Give the extent of all uninfected red blood cells.
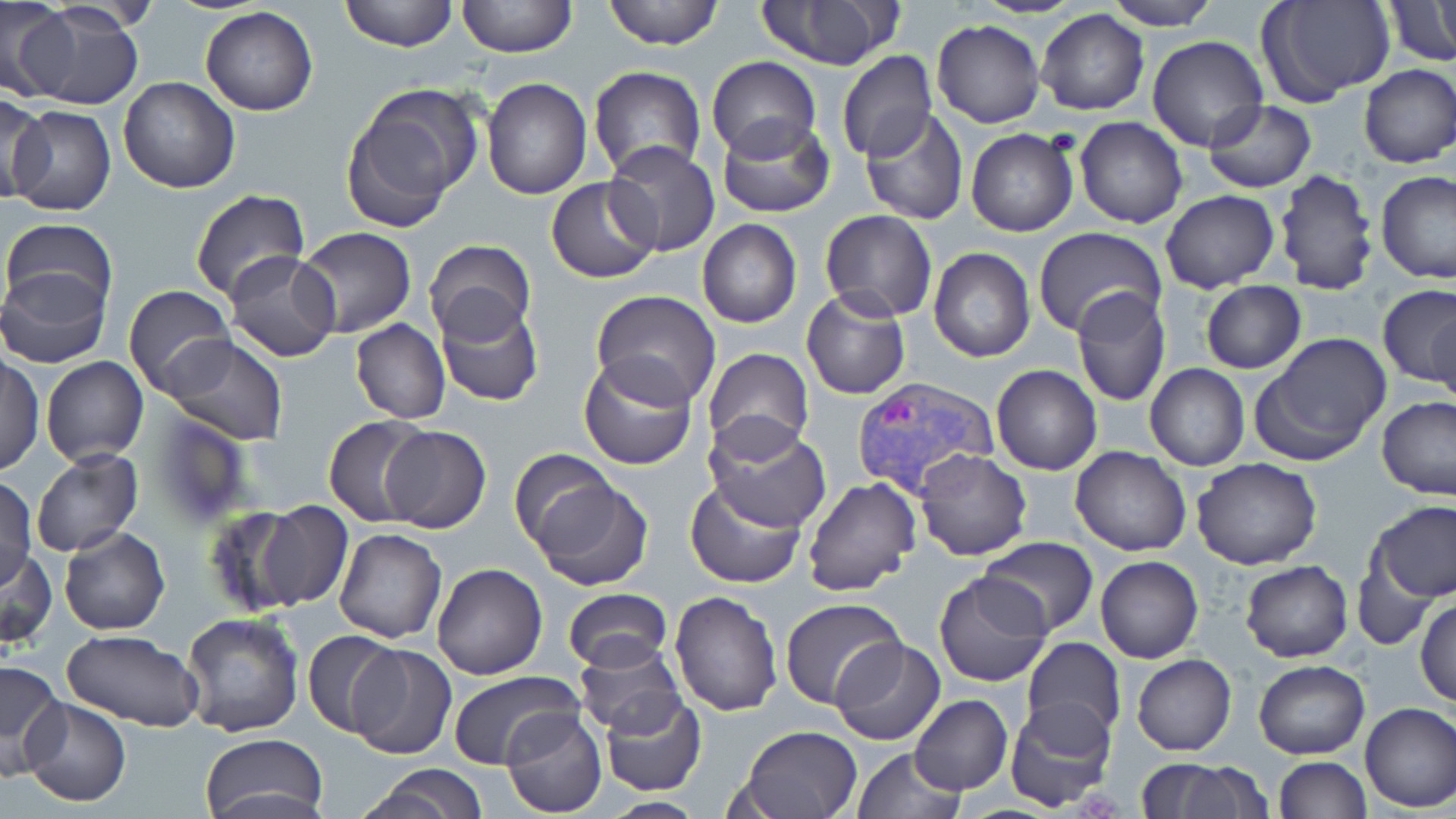
Approximate bounding boxes as (x1, y1, x2, y2) in pixels.
Uninfected red blood cells: (340, 0, 457, 51), (456, 0, 578, 60), (601, 0, 726, 50), (972, 0, 1083, 19), (1106, 0, 1220, 29), (1260, 0, 1395, 109), (1382, 0, 1456, 68), (0, 1, 74, 102), (18, 1, 144, 111), (751, 1, 898, 71), (201, 7, 317, 115), (1036, 8, 1149, 116), (932, 21, 1044, 129), (1148, 36, 1269, 152), (836, 52, 937, 162), (706, 56, 821, 162), (1356, 64, 1455, 168), (588, 65, 706, 179), (118, 76, 239, 193), (482, 77, 593, 200), (340, 85, 481, 227), (0, 93, 53, 202), (1202, 100, 1318, 195), (8, 104, 116, 216), (858, 110, 969, 225), (715, 114, 836, 218), (1074, 117, 1187, 229), (966, 130, 1077, 237), (603, 141, 722, 257), (1273, 167, 1380, 296), (1377, 170, 1456, 285), (545, 177, 659, 284), (187, 189, 312, 307), (1161, 190, 1281, 293), (820, 210, 937, 321), (2, 216, 117, 314), (697, 219, 802, 328), (295, 227, 416, 338), (1032, 227, 1167, 341), (424, 239, 536, 346), (929, 247, 1035, 362), (223, 250, 342, 363), (0, 268, 112, 368), (1199, 281, 1308, 374), (1379, 284, 1456, 388), (122, 285, 238, 398), (800, 288, 912, 400), (1072, 288, 1172, 406), (591, 291, 721, 408), (435, 299, 545, 408), (1429, 302, 1456, 412), (350, 319, 451, 424), (1251, 333, 1392, 466), (162, 335, 289, 445), (704, 347, 814, 456), (577, 353, 698, 469), (1, 354, 44, 478), (41, 356, 148, 465), (991, 364, 1103, 475), (1145, 364, 1249, 471), (1378, 398, 1456, 501), (144, 412, 254, 530), (324, 415, 433, 527), (706, 420, 831, 534), (378, 425, 492, 533), (1070, 446, 1191, 557), (509, 448, 618, 552), (29, 449, 144, 558), (914, 449, 1033, 561), (1192, 457, 1322, 570), (525, 472, 654, 591), (1, 476, 37, 587), (802, 476, 923, 599), (685, 478, 807, 588), (252, 500, 353, 611), (1369, 502, 1455, 602), (200, 504, 315, 616), (59, 527, 169, 635), (334, 527, 447, 643), (978, 536, 1100, 636), (0, 546, 57, 650), (1346, 552, 1439, 651), (1095, 555, 1204, 664), (1240, 560, 1352, 663), (431, 563, 547, 679), (932, 571, 1053, 686), (562, 589, 673, 673), (669, 589, 783, 716), (1415, 597, 1456, 706), (780, 598, 905, 711), (179, 612, 306, 738), (301, 629, 403, 739), (62, 630, 205, 730), (32, 635, 180, 791), (572, 635, 686, 737), (829, 637, 944, 747), (1021, 637, 1126, 746), (348, 643, 457, 760), (1131, 653, 1237, 755), (1254, 660, 1369, 760), (0, 661, 68, 777), (447, 669, 586, 770), (599, 692, 707, 796), (909, 693, 1012, 795), (21, 697, 130, 806), (1004, 698, 1116, 811), (1358, 701, 1456, 813), (500, 707, 608, 816), (733, 725, 862, 819), (198, 734, 330, 819), (851, 746, 965, 819), (1274, 756, 1371, 818), (1144, 761, 1270, 819), (358, 765, 489, 819), (593, 796, 709, 818).

{
  "slide_level_diagnosis": "Plasmodium vivax",
  "preparation": "thin blood smear",
  "magnification": "1000x",
  "field_of_view": "one of a larger specimen",
  "modality": "light microscopy",
  "plasmodium_vivax_infected_red_blood_cell_locations": "approximate bounding boxes as (x1, y1, x2, y2) in pixels: (850, 376, 1000, 499)",
  "image_size": "1456×819 pixels",
  "stain": "May-Grünwald-Giemsa"
}